Locate and identify every blood parasite.
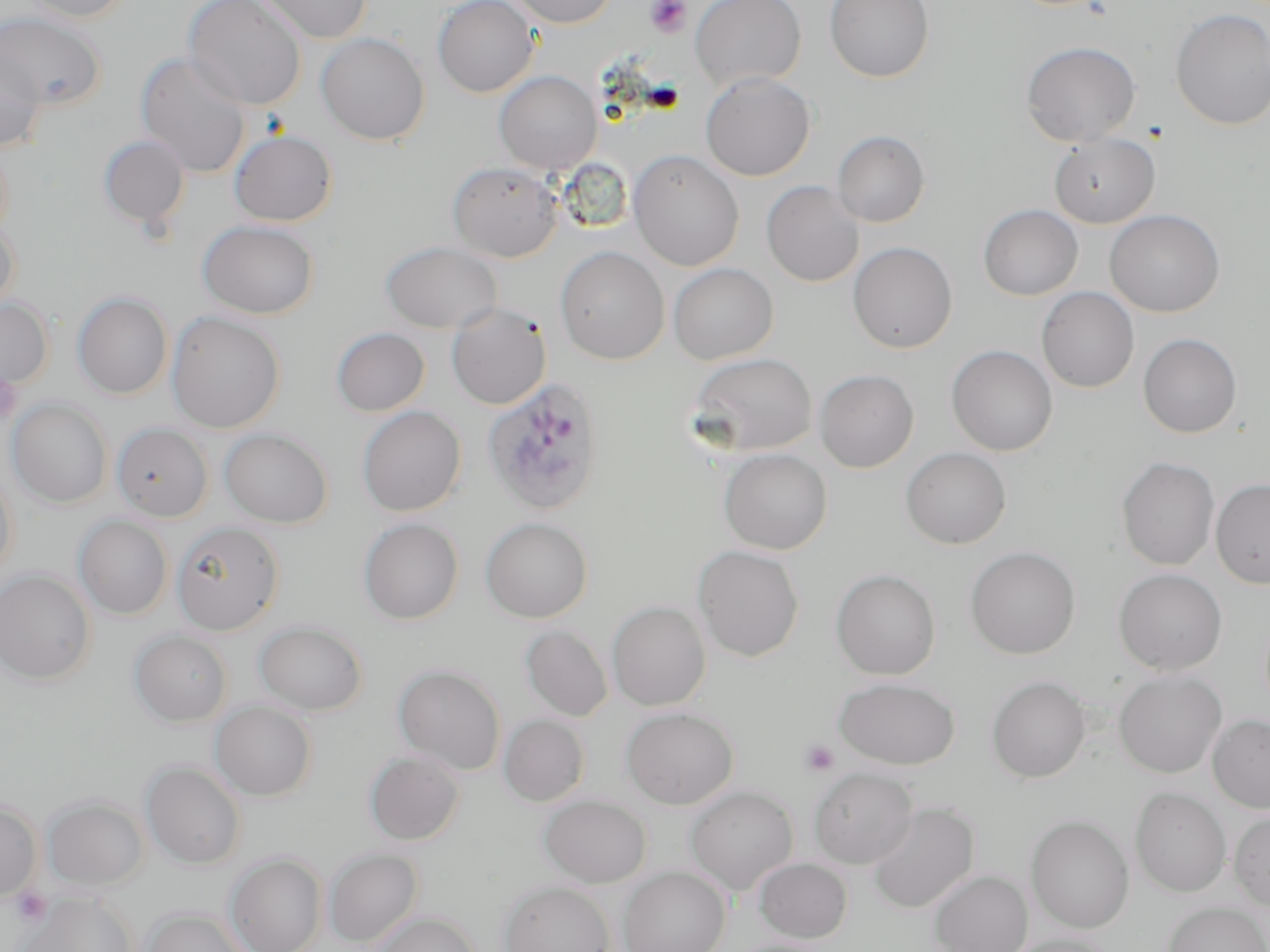
Approximate bounding boxes as named x1/y1/x2/y2 corners in pixels.
Plasmodium ovale-infected red blood cells: (x1=482, y1=378, x2=606, y2=516).
No Plasmodium falciparum, Plasmodium malariae, Plasmodium vivax, Babesia divergens, or Trypanosoma brucei observed.

Platelet locations: (x1=645, y1=0, x2=692, y2=37), (x1=0, y1=369, x2=21, y2=428), (x1=800, y1=739, x2=840, y2=776), (x1=12, y1=887, x2=52, y2=926). Uninfected red blood cell locations: (x1=20, y1=0, x2=133, y2=23), (x1=183, y1=0, x2=306, y2=111), (x1=254, y1=0, x2=373, y2=44), (x1=432, y1=0, x2=539, y2=97), (x1=507, y1=0, x2=618, y2=28), (x1=690, y1=0, x2=807, y2=91), (x1=824, y1=0, x2=934, y2=82), (x1=1170, y1=8, x2=1270, y2=130), (x1=0, y1=11, x2=106, y2=110), (x1=316, y1=32, x2=430, y2=145), (x1=1020, y1=42, x2=1141, y2=147), (x1=0, y1=48, x2=46, y2=151), (x1=135, y1=53, x2=252, y2=178), (x1=494, y1=70, x2=602, y2=174), (x1=700, y1=72, x2=816, y2=181), (x1=229, y1=129, x2=338, y2=227), (x1=832, y1=130, x2=930, y2=227), (x1=1049, y1=133, x2=1161, y2=229), (x1=98, y1=134, x2=190, y2=231), (x1=0, y1=141, x2=13, y2=242), (x1=628, y1=150, x2=744, y2=271), (x1=447, y1=162, x2=562, y2=262), (x1=761, y1=180, x2=864, y2=287), (x1=978, y1=204, x2=1083, y2=300), (x1=1104, y1=209, x2=1225, y2=317), (x1=0, y1=220, x2=21, y2=316), (x1=197, y1=220, x2=319, y2=319), (x1=380, y1=241, x2=502, y2=334), (x1=848, y1=241, x2=957, y2=353), (x1=555, y1=246, x2=670, y2=365), (x1=668, y1=262, x2=779, y2=365), (x1=1036, y1=287, x2=1139, y2=392), (x1=72, y1=292, x2=173, y2=399), (x1=0, y1=298, x2=53, y2=391), (x1=446, y1=302, x2=551, y2=410), (x1=165, y1=311, x2=285, y2=433), (x1=330, y1=327, x2=430, y2=416), (x1=1137, y1=333, x2=1242, y2=438), (x1=946, y1=345, x2=1057, y2=456), (x1=688, y1=352, x2=817, y2=457), (x1=815, y1=369, x2=919, y2=473), (x1=7, y1=398, x2=112, y2=508), (x1=357, y1=406, x2=466, y2=516), (x1=111, y1=422, x2=213, y2=521), (x1=219, y1=428, x2=333, y2=528), (x1=900, y1=447, x2=1011, y2=549), (x1=719, y1=448, x2=832, y2=554), (x1=1116, y1=456, x2=1220, y2=571), (x1=0, y1=468, x2=19, y2=579), (x1=1210, y1=479, x2=1270, y2=589), (x1=74, y1=515, x2=173, y2=619), (x1=480, y1=517, x2=593, y2=623), (x1=358, y1=518, x2=463, y2=625), (x1=172, y1=521, x2=284, y2=635), (x1=693, y1=545, x2=805, y2=662), (x1=965, y1=546, x2=1081, y2=659), (x1=831, y1=568, x2=940, y2=679), (x1=1113, y1=568, x2=1228, y2=675), (x1=0, y1=569, x2=95, y2=684), (x1=607, y1=601, x2=711, y2=711), (x1=254, y1=620, x2=368, y2=715), (x1=520, y1=625, x2=613, y2=722), (x1=129, y1=630, x2=233, y2=726), (x1=393, y1=664, x2=506, y2=775), (x1=1113, y1=669, x2=1227, y2=777), (x1=987, y1=675, x2=1090, y2=783), (x1=833, y1=676, x2=960, y2=769), (x1=210, y1=701, x2=317, y2=801), (x1=621, y1=707, x2=738, y2=809), (x1=1208, y1=714, x2=1270, y2=812), (x1=499, y1=715, x2=589, y2=806), (x1=364, y1=750, x2=465, y2=845), (x1=141, y1=760, x2=246, y2=870), (x1=809, y1=768, x2=918, y2=868), (x1=685, y1=786, x2=798, y2=894), (x1=1131, y1=787, x2=1231, y2=897), (x1=539, y1=795, x2=652, y2=887), (x1=42, y1=796, x2=149, y2=891), (x1=0, y1=800, x2=42, y2=900), (x1=866, y1=802, x2=979, y2=914), (x1=1229, y1=811, x2=1270, y2=912), (x1=1026, y1=814, x2=1134, y2=933), (x1=323, y1=848, x2=423, y2=947), (x1=225, y1=853, x2=327, y2=952), (x1=753, y1=857, x2=853, y2=943), (x1=619, y1=866, x2=730, y2=952), (x1=929, y1=870, x2=1033, y2=952), (x1=498, y1=880, x2=615, y2=952), (x1=22, y1=893, x2=137, y2=952), (x1=1162, y1=901, x2=1270, y2=952), (x1=141, y1=908, x2=251, y2=952), (x1=370, y1=911, x2=483, y2=952), (x1=1005, y1=934, x2=1118, y2=952). Slide-level diagnosis: Plasmodium ovale. Light microscopy. One field of a larger specimen. Image is 1270×952 pixels. 1000x magnification. May-Grünwald-Giemsa stain. Thin blood smear.